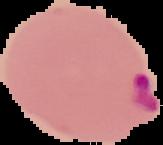

preparation = thin blood film
malaria status = parasitized
image size = 163×145 pixels
image type = cell region segmented out of the field of view; surrounding area masked to black